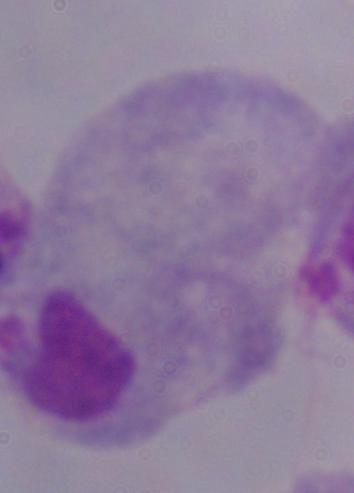
Photomicrograph. A trichomonad is shown. Captured at 1000x magnification.